Classify this cell by malaria status.
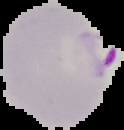

Parasitized.

Image is 124×130 pixels. Segmented cell region on a black background. From a thin blood smear.